Report the malaria status of this cell.
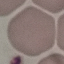
Uninfected.

preparation = thin blood smear
capture = smartphone camera at the microscope eyepiece
stain = Giemsa
image type = cell patch, automatically extracted from a larger field of view and resized to 64 × 64 pixels